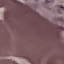
malaria status = uninfected
stain = Giemsa
image type = automatically extracted cell patch, resized to 64 × 64 pixels
preparation = thin smear
capture = smartphone camera at the microscope eyepiece